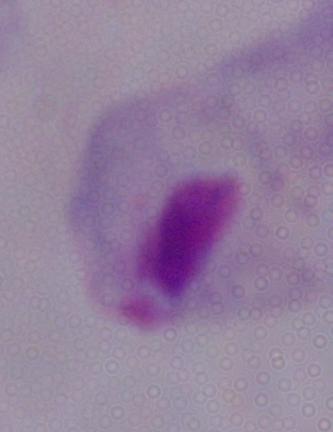

Summary:
  - Modality: photomicrograph
  - Identification: trichomonad
  - Magnification: 1000x